Report the malaria status of this cell.
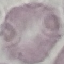
It is uninfected.

preparation = thin blood film
image type = cell patch, automatically extracted from a larger field of view and resized to 64 × 64 pixels
stain = Giemsa
capture = smartphone camera at the microscope eyepiece